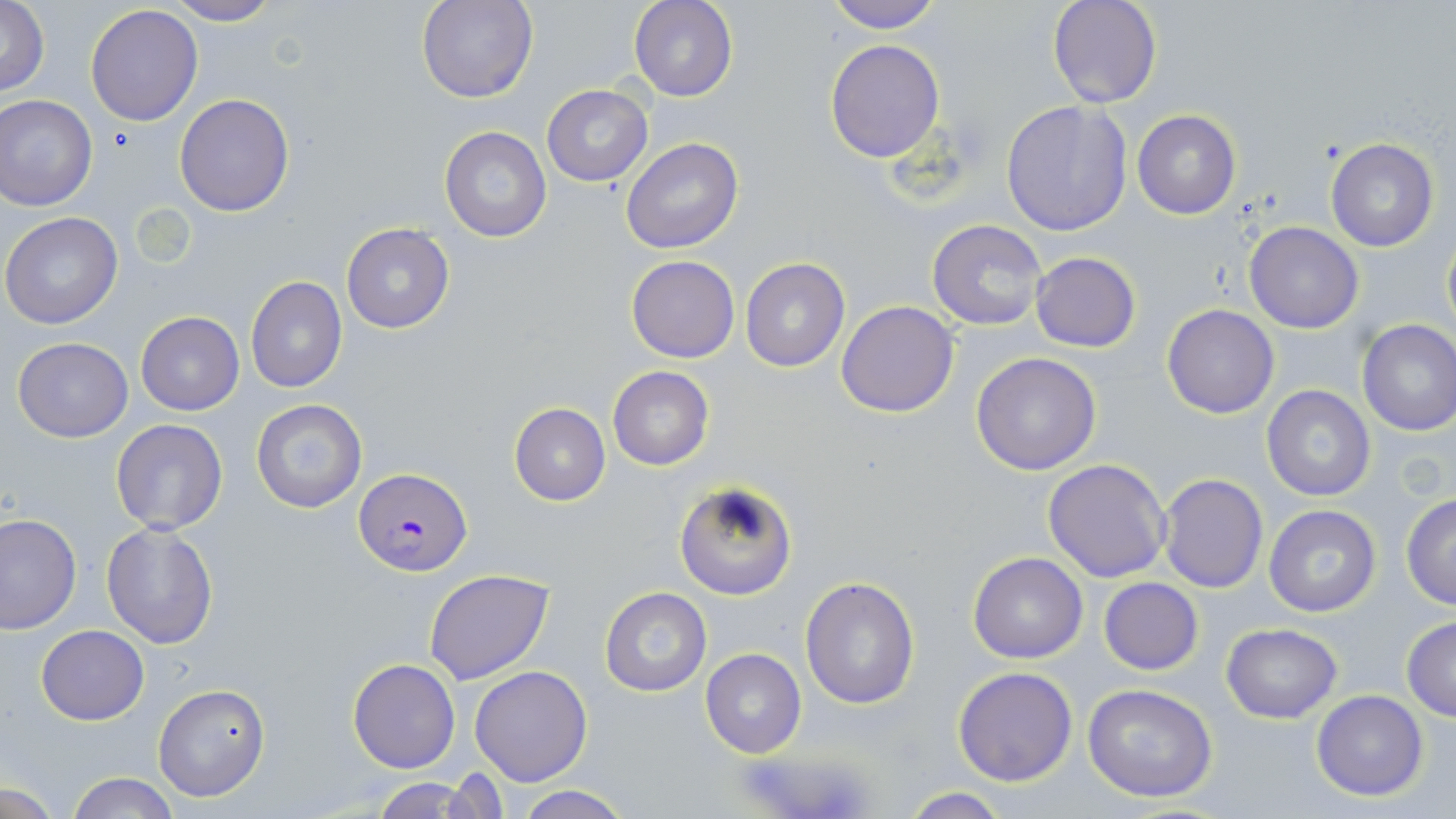

Summary:
  - Coordinate format: approximate bounding boxes as named x1/y1/x2/y2 corners in pixels
  - Platelet locations: (x1=108, y1=126, x2=140, y2=155)
  - Plasmodium falciparum-infected red blood cell locations: (x1=355, y1=468, x2=472, y2=577)
  - Uninfected red blood cell locations: (x1=417, y1=0, x2=538, y2=104), (x1=629, y1=0, x2=738, y2=102), (x1=820, y1=0, x2=945, y2=34), (x1=1046, y1=0, x2=1162, y2=109), (x1=163, y1=1, x2=281, y2=25), (x1=1, y1=2, x2=50, y2=97), (x1=85, y1=5, x2=203, y2=126), (x1=824, y1=38, x2=945, y2=162), (x1=542, y1=85, x2=653, y2=186), (x1=174, y1=93, x2=294, y2=216), (x1=0, y1=95, x2=98, y2=211), (x1=1001, y1=99, x2=1133, y2=235), (x1=1132, y1=109, x2=1241, y2=220), (x1=439, y1=126, x2=552, y2=243), (x1=1325, y1=137, x2=1439, y2=253), (x1=622, y1=138, x2=743, y2=254), (x1=1, y1=212, x2=124, y2=330), (x1=927, y1=218, x2=1048, y2=332), (x1=1244, y1=221, x2=1364, y2=333), (x1=340, y1=222, x2=455, y2=333), (x1=1442, y1=224, x2=1455, y2=341), (x1=1030, y1=252, x2=1142, y2=354), (x1=625, y1=254, x2=741, y2=364), (x1=740, y1=257, x2=851, y2=372), (x1=246, y1=276, x2=348, y2=393), (x1=837, y1=301, x2=959, y2=418), (x1=1161, y1=304, x2=1280, y2=419), (x1=136, y1=311, x2=244, y2=415), (x1=1356, y1=318, x2=1456, y2=436), (x1=12, y1=336, x2=133, y2=441), (x1=971, y1=351, x2=1103, y2=476), (x1=607, y1=366, x2=713, y2=471), (x1=1260, y1=385, x2=1377, y2=501), (x1=250, y1=398, x2=369, y2=514), (x1=509, y1=403, x2=610, y2=506), (x1=110, y1=419, x2=229, y2=535), (x1=1043, y1=458, x2=1172, y2=582), (x1=1157, y1=473, x2=1268, y2=592), (x1=674, y1=481, x2=798, y2=600), (x1=1400, y1=493, x2=1456, y2=610), (x1=1262, y1=503, x2=1382, y2=619), (x1=0, y1=513, x2=81, y2=634), (x1=101, y1=522, x2=218, y2=648), (x1=966, y1=552, x2=1088, y2=663), (x1=424, y1=569, x2=554, y2=684), (x1=800, y1=577, x2=920, y2=708), (x1=1099, y1=578, x2=1203, y2=674), (x1=600, y1=586, x2=711, y2=696), (x1=1401, y1=616, x2=1456, y2=721), (x1=1220, y1=622, x2=1343, y2=723), (x1=36, y1=625, x2=149, y2=725), (x1=701, y1=648, x2=806, y2=760), (x1=348, y1=658, x2=459, y2=773), (x1=469, y1=666, x2=594, y2=786), (x1=952, y1=666, x2=1078, y2=787), (x1=154, y1=684, x2=270, y2=802), (x1=1081, y1=684, x2=1220, y2=803), (x1=1310, y1=690, x2=1429, y2=802), (x1=67, y1=773, x2=178, y2=819), (x1=371, y1=777, x2=486, y2=819), (x1=2, y1=781, x2=62, y2=817), (x1=509, y1=786, x2=634, y2=819), (x1=896, y1=788, x2=1017, y2=818)
  - Slide-level diagnosis: Plasmodium falciparum
  - Field of view: single
  - Modality: light microscopy
  - Magnification: 1000x
  - Preparation: thin blood film
  - Image size: 1456×819 pixels
  - Stain: May-Grünwald-Giemsa